Assess this cell for malaria.
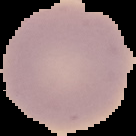
It is uninfected.

image size = 136×136 pixels
image type = cell region segmented out of the field of view; surrounding area masked to black
preparation = thin blood smear